Report the malaria status of this cell.
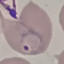

It is parasitized.

Thin smear of blood. Giemsa stain. Cell patch, automatically extracted from a larger field of view and resized to 64 × 64 pixels. Photographed with a smartphone camera at the microscope eyepiece.